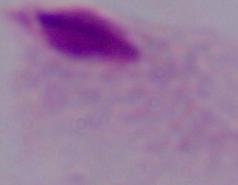
Summary:
  - Modality: photomicrograph
  - Magnification: 1000x
  - Identification: trichomonad